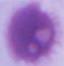
identification: red blood cell
modality: photomicrograph
magnification: 1000x